Identify the parasite.
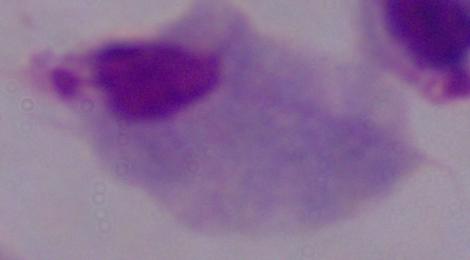
This is a trichomonad.

modality: photomicrograph
magnification: 1000x